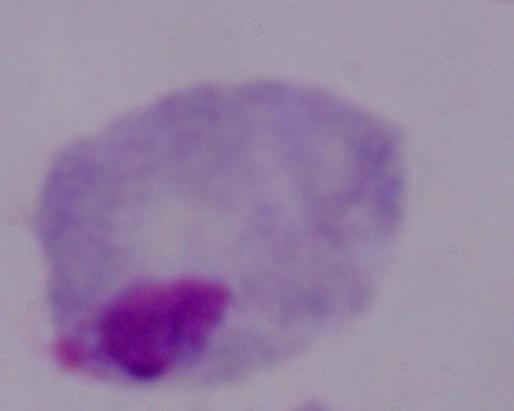
Summary:
  - Modality: photomicrograph
  - Magnification: 1000x
  - Identification: trichomonad